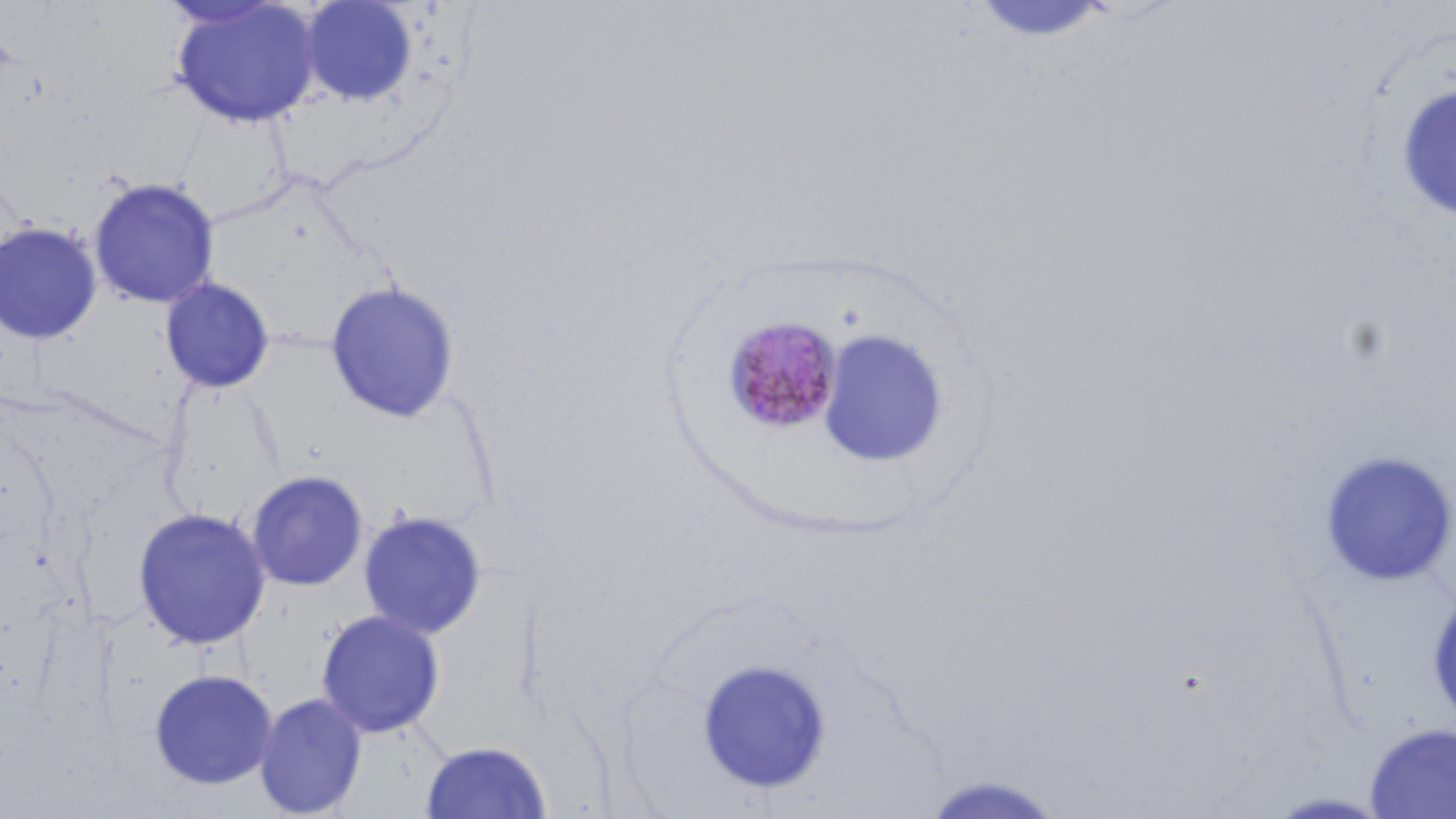

Summary:
  - Coordinate format: approximate bounding boxes as (x1,y1)-(x2,y2) corner pairs in pixels
  - Uninfected red blood cell locations: (298,0)-(419,106), (168,1)-(323,129), (969,1)-(1113,45), (1394,83)-(1456,223), (88,177)-(221,310), (0,221)-(103,345), (159,276)-(276,395), (325,280)-(460,424), (1319,451)-(1456,587), (245,469)-(370,592), (131,506)-(272,650), (358,510)-(488,640), (1427,588)-(1456,727), (315,609)-(446,739), (695,657)-(832,794), (147,668)-(279,791), (254,692)-(368,818), (1363,723)-(1456,818), (418,740)-(552,818), (916,774)-(1071,818), (1262,790)-(1396,818)
  - Plasmodium malariae-infected red blood cell locations: (723,316)-(844,435)
  - Slide-level diagnosis: Plasmodium malariae
  - Modality: optical microscopy
  - Stain: May-Grünwald-Giemsa
  - Image size: 1456×819 pixels
  - Preparation: thin blood smear
  - Magnification: 1000x
  - Field of view: one of a larger specimen